Assess this cell for malaria.
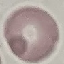
Uninfected.

Summary:
  - Capture: smartphone camera at the microscope eyepiece
  - Image type: automatically extracted cell patch, resized to 64 × 64 pixels
  - Stain: Giemsa
  - Preparation: thin blood smear